Assess the morphology of the erythrocytes.
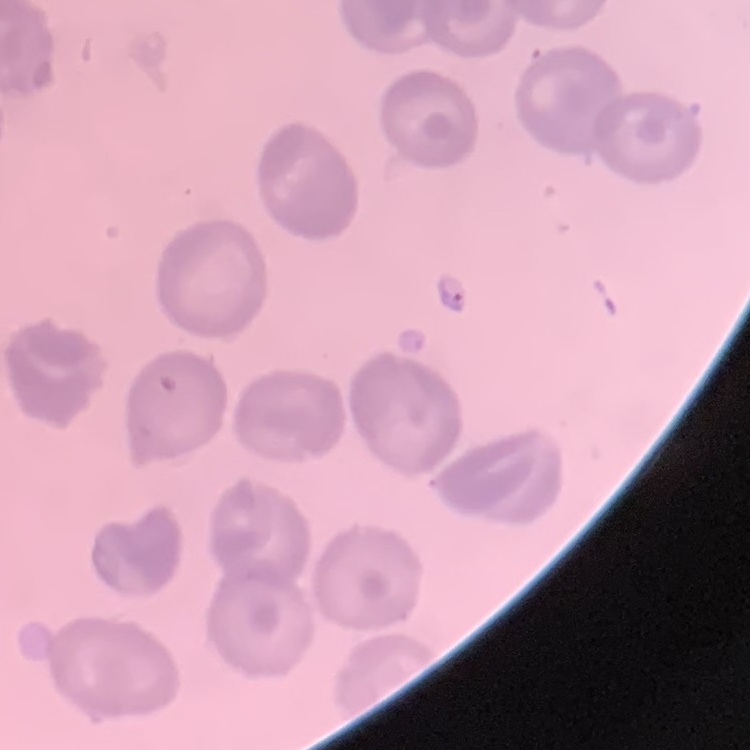
They show no rouleaux formation.

Summary:
  - Image type: one tile cut from a larger photomicrograph
  - Stain: Field's or Giemsa
  - Preparation: thin blood film